Identify the parasite.
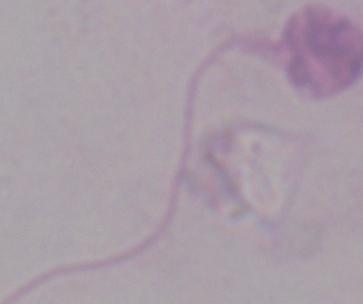

Leishmania.

Photomicrograph. Captured at 1000x magnification.